Locate every Plasmodium falciparum parasite and give its life-cycle stage, and locate every leukocyte and any debris.
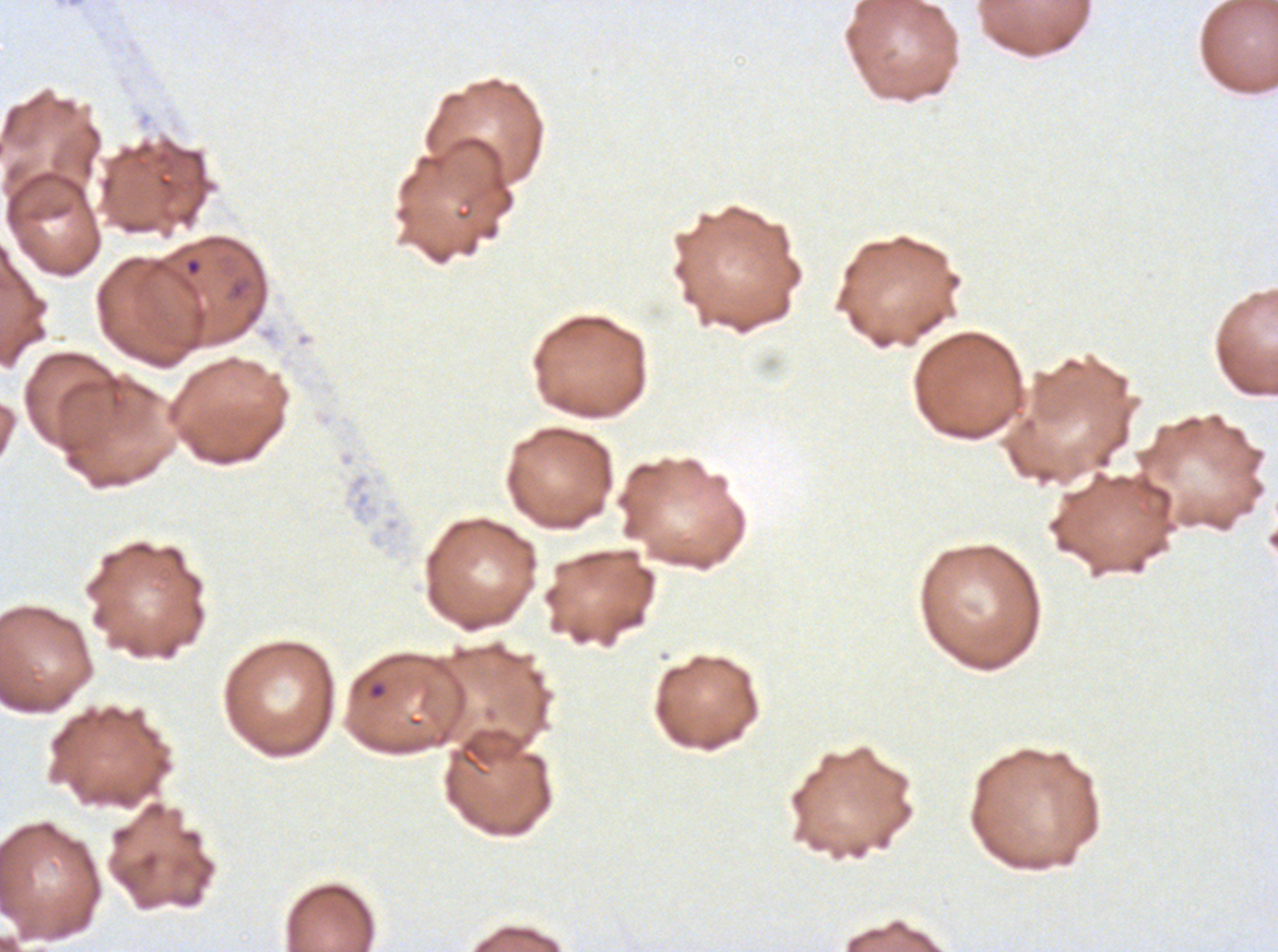
Approximate bounding boxes as {x1, y1, x2, y2} in pixels.
Rings: {367, 680, 387, 701}.
Debris: {183, 255, 203, 278}.
No late-ring/early-trophozoite forms, mid trophozoites, late trophozoites, early schizonts, late schizonts, segmenters, gametocytes, or leukocytes observed.

Summary:
  - Image size: 1278×952 pixels
  - Preparation: thin blood film
  - Stain: Giemsa
  - Specimen: ex-vivo Plasmodium falciparum culture from a patient in The Gambia, grown for 24 to 48 hours
  - Field of view: sub-image separated from a larger composite